Outline each blood parasite and name the species.
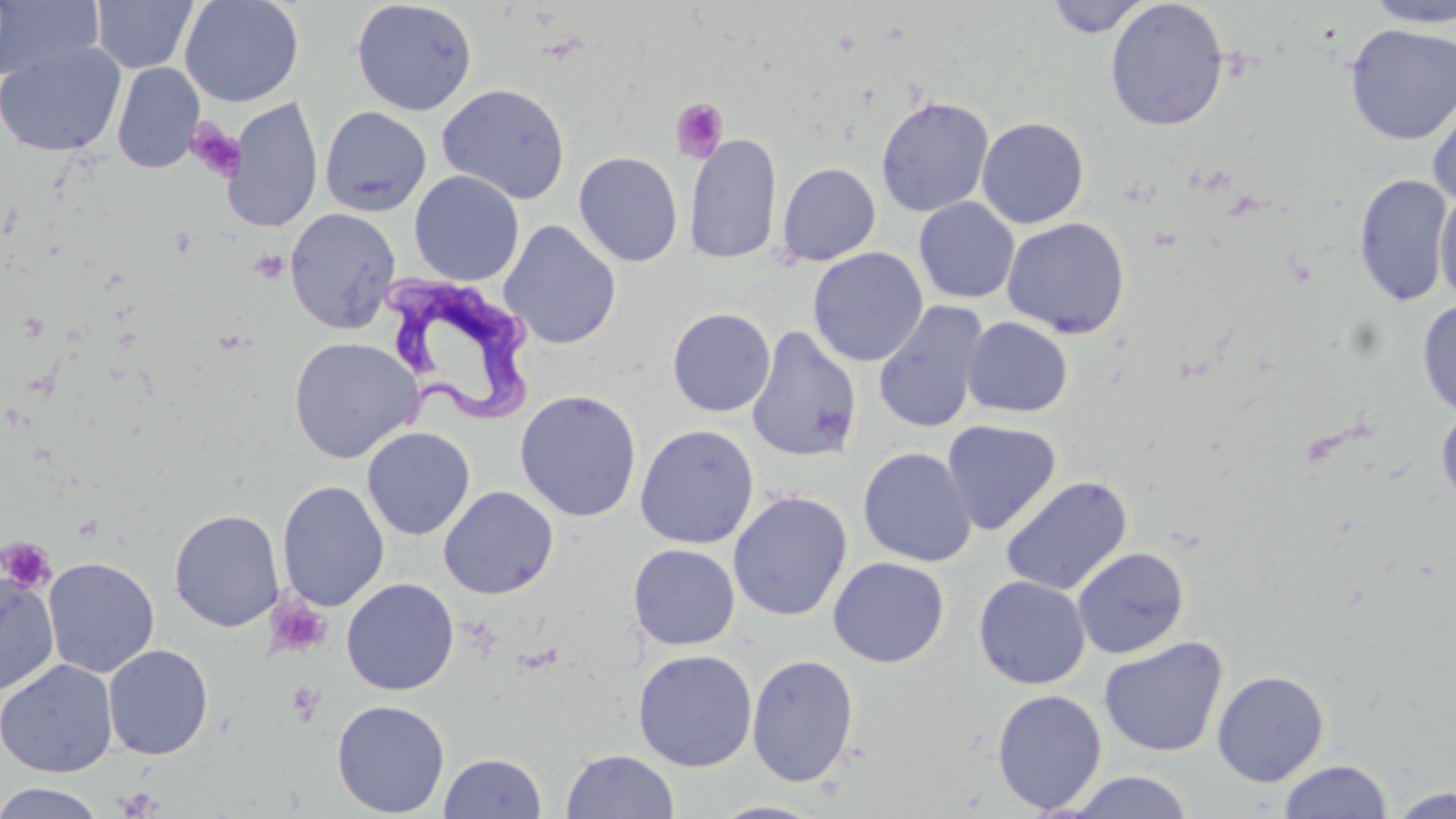
Approximate bounding boxes as named x1/y1/x2/y2 corners in pixels.
Trypanosoma brucei: (x1=380, y1=273, x2=536, y2=425).
No Plasmodium falciparum, Plasmodium ovale, Plasmodium malariae, Plasmodium vivax, or Babesia divergens observed.

Platelet locations: (x1=670, y1=97, x2=728, y2=162), (x1=186, y1=119, x2=245, y2=185), (x1=249, y1=249, x2=289, y2=285), (x1=1, y1=536, x2=57, y2=593), (x1=267, y1=597, x2=332, y2=659), (x1=285, y1=679, x2=326, y2=726), (x1=115, y1=787, x2=162, y2=817). Uninfected red blood cell locations: (x1=91, y1=0, x2=198, y2=74), (x1=180, y1=0, x2=304, y2=107), (x1=1046, y1=0, x2=1151, y2=38), (x1=0, y1=1, x2=103, y2=82), (x1=351, y1=1, x2=477, y2=116), (x1=1105, y1=1, x2=1229, y2=131), (x1=1361, y1=1, x2=1456, y2=28), (x1=1343, y1=22, x2=1456, y2=146), (x1=0, y1=42, x2=125, y2=158), (x1=112, y1=62, x2=205, y2=174), (x1=436, y1=83, x2=571, y2=204), (x1=1428, y1=86, x2=1456, y2=208), (x1=875, y1=95, x2=994, y2=217), (x1=223, y1=97, x2=323, y2=234), (x1=320, y1=106, x2=432, y2=216), (x1=976, y1=116, x2=1090, y2=229), (x1=684, y1=132, x2=782, y2=265), (x1=574, y1=151, x2=684, y2=267), (x1=776, y1=162, x2=881, y2=266), (x1=409, y1=171, x2=524, y2=286), (x1=1353, y1=174, x2=1453, y2=307), (x1=1434, y1=187, x2=1456, y2=305), (x1=914, y1=197, x2=1019, y2=304), (x1=285, y1=208, x2=401, y2=334), (x1=1002, y1=217, x2=1131, y2=338), (x1=500, y1=220, x2=621, y2=351), (x1=808, y1=247, x2=928, y2=367), (x1=1417, y1=299, x2=1456, y2=417), (x1=872, y1=301, x2=990, y2=434), (x1=667, y1=307, x2=776, y2=417), (x1=961, y1=317, x2=1073, y2=418), (x1=746, y1=325, x2=862, y2=462), (x1=288, y1=336, x2=423, y2=464), (x1=515, y1=389, x2=642, y2=522), (x1=1436, y1=406, x2=1456, y2=508), (x1=941, y1=420, x2=1061, y2=536), (x1=634, y1=424, x2=760, y2=549), (x1=361, y1=427, x2=475, y2=540), (x1=858, y1=446, x2=977, y2=567), (x1=1000, y1=476, x2=1132, y2=596), (x1=277, y1=481, x2=390, y2=612), (x1=438, y1=486, x2=559, y2=599), (x1=728, y1=490, x2=852, y2=621), (x1=168, y1=509, x2=284, y2=632), (x1=628, y1=543, x2=740, y2=650), (x1=1072, y1=546, x2=1190, y2=659), (x1=43, y1=556, x2=159, y2=678), (x1=828, y1=557, x2=950, y2=668), (x1=0, y1=572, x2=60, y2=697), (x1=973, y1=576, x2=1090, y2=689), (x1=341, y1=578, x2=459, y2=696), (x1=1098, y1=636, x2=1229, y2=758), (x1=103, y1=644, x2=213, y2=759), (x1=632, y1=649, x2=758, y2=772), (x1=746, y1=653, x2=860, y2=788), (x1=0, y1=659, x2=117, y2=778), (x1=1211, y1=670, x2=1329, y2=786), (x1=991, y1=689, x2=1108, y2=814), (x1=332, y1=699, x2=450, y2=817), (x1=561, y1=749, x2=680, y2=818), (x1=439, y1=752, x2=547, y2=818), (x1=1279, y1=759, x2=1392, y2=818), (x1=1065, y1=770, x2=1194, y2=818), (x1=0, y1=782, x2=107, y2=819), (x1=1387, y1=787, x2=1455, y2=818), (x1=707, y1=800, x2=831, y2=818). Slide-level diagnosis: Trypanosoma brucei. Captured at 1000x magnification. Image is 1456×819 pixels. Optical microscopy. May-Grünwald-Giemsa-stained preparation. Thin blood smear. Single field of view.